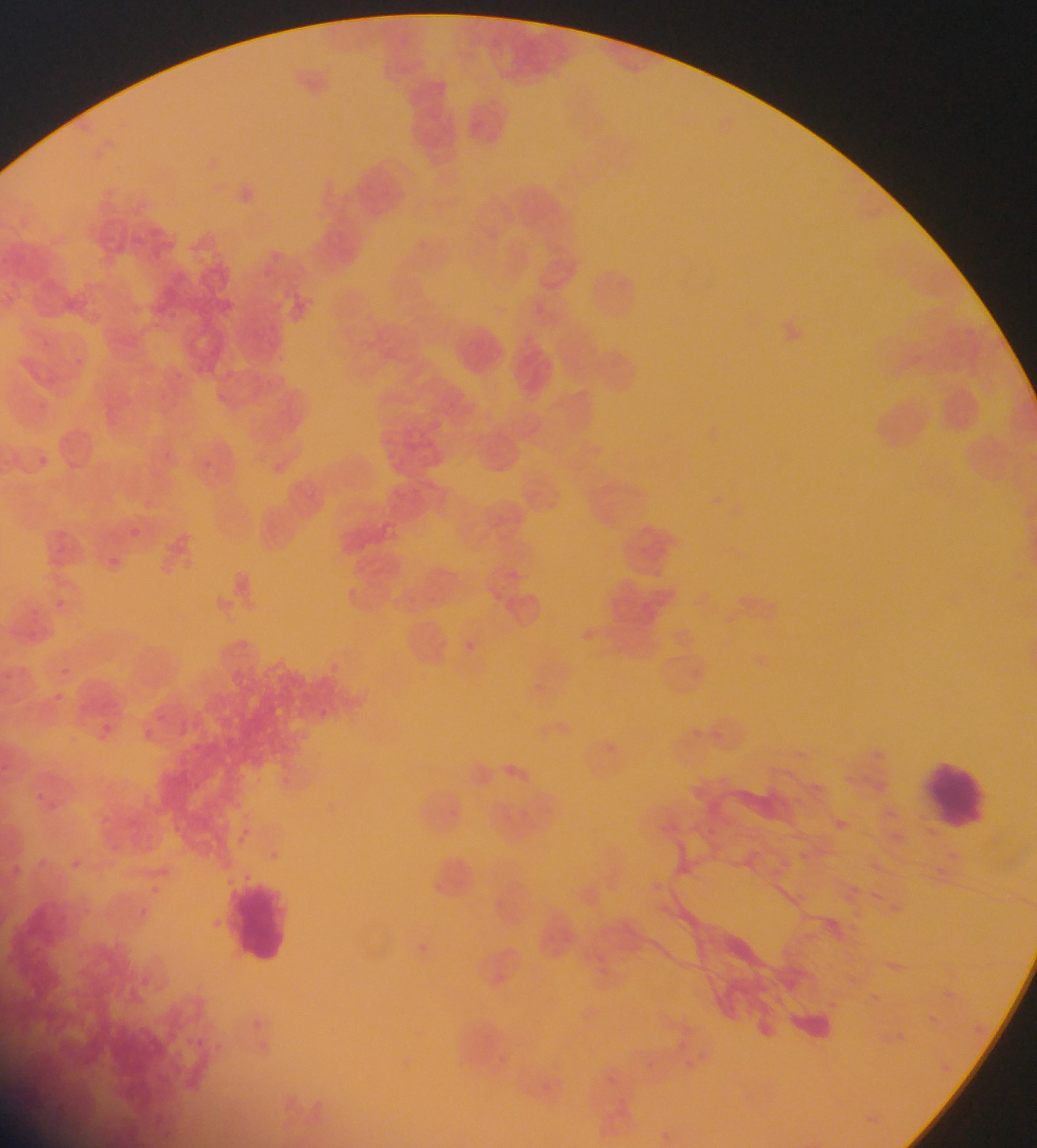

image_size: 1037×1148 pixels
country: Ghana
field_of_view: single
preparation: thin blood smear
plasmodium_parasite_locations: 'approximate bounding boxes as {left, top, right, bottom} in pixels: {130, 528, 139, 537}, {107, 553, 128, 567}, {463, 636, 475, 643}, {55, 691, 68, 704}, {98, 718, 106, 726}, {137, 725, 155, 741}, {32, 782, 52, 806}, {227, 825, 255, 850}, {68, 857, 82, 870}, {12, 865, 21, 874}, {146, 879, 169, 900}'
leukocyte_locations: 'approximate bounding boxes as {left, top, right, bottom} in pixels: {921, 751, 992, 835}, {228, 877, 294, 966}'
capture: mobile-phone photograph through a microscope